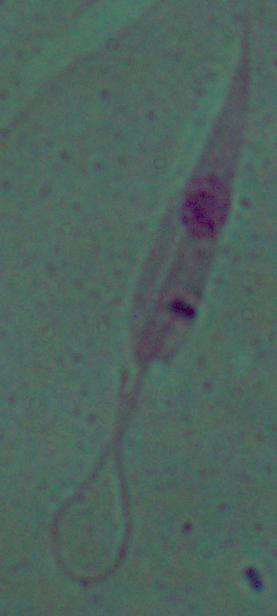
Captured at 1000x magnification. A Leishmania parasite is seen. Photomicrograph.